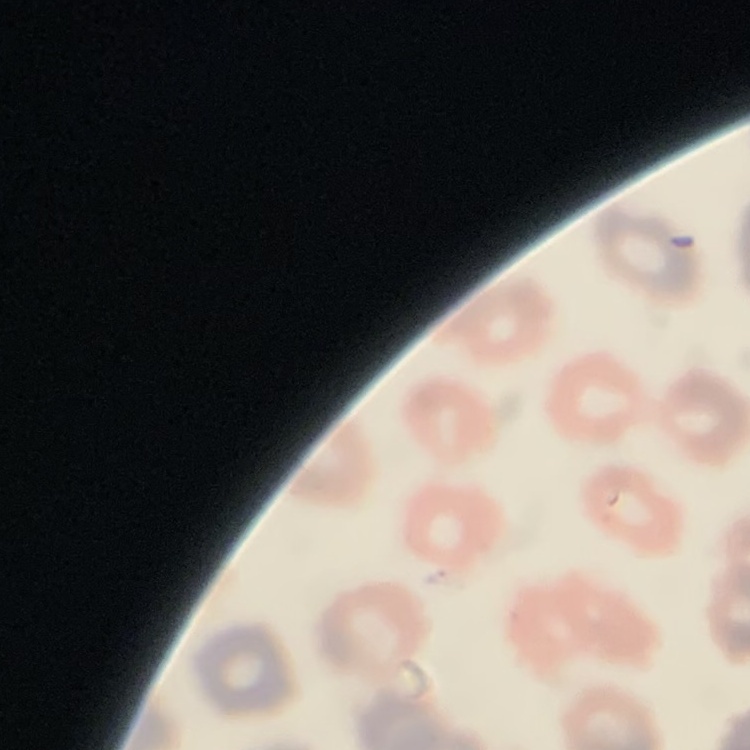
The erythrocytes exhibit no rouleaux formation. Stained with either Field's or Giemsa. Square crop of a larger photomicrograph. Thin peripheral smear.